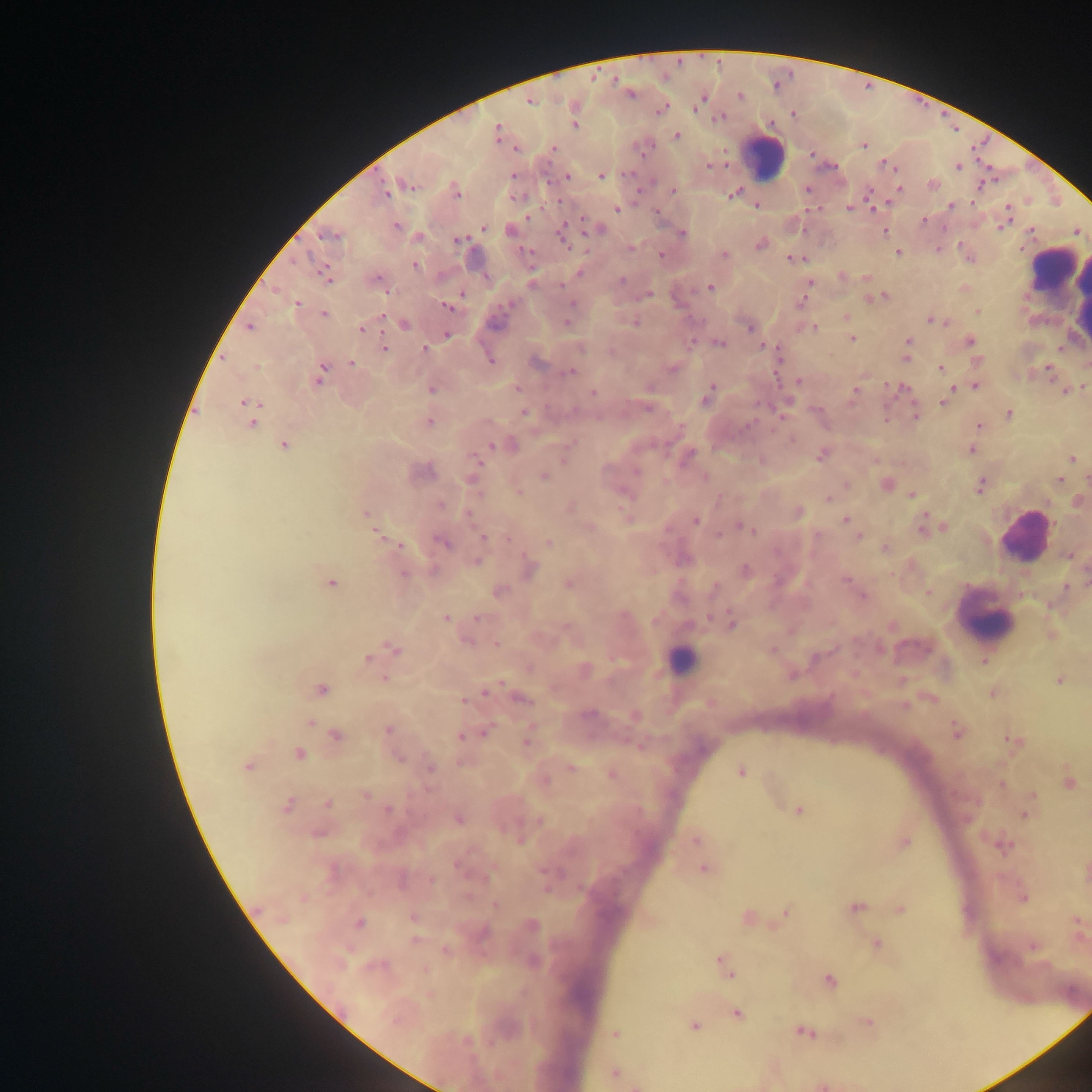

Approximate centers as x y in pixels. Malaria parasite locations: 630 94; 529 101; 662 109; 573 116; 718 117; 574 124; 497 133; 676 135; 863 144; 552 148; 811 154; 958 166; 567 176; 601 176; 407 184; 933 185; 672 190; 898 190; 456 191; 733 193; 756 205; 952 206; 850 208; 616 209; 1007 209; 924 221; 1004 222; 396 226; 483 227; 596 229; 510 230; 884 231; 562 232; 330 234; 682 234; 418 237; 459 239; 760 244; 898 252; 660 255; 723 255; 968 256; 796 259; 415 265; 325 275; 841 275; 865 278; 376 279; 622 280; 809 283; 710 287; 648 294; 874 297; 801 301; 296 304; 449 306; 978 312; 324 313; 845 317; 568 320; 931 320; 403 323; 249 326; 750 327; 361 328; 812 328; 446 334; 851 338; 908 341; 970 341; 717 342; 384 347; 579 347; 424 349; 906 356; 490 358; 977 360; 352 363; 940 368; 672 369; 1048 370; 569 372; 321 374; 797 382; 975 386; 1083 386; 517 387; 430 388; 899 388; 1066 390; 854 391; 593 393; 708 394; 947 397; 943 401; 249 405; 647 406; 525 412; 1008 414; 915 415; 251 419; 429 422; 979 426; 791 440; 283 444; 509 445; 971 449; 822 454; 686 456; 1072 459; 761 460; 476 461; 420 470; 543 475; 473 479; 1059 479; 886 484; 845 485; 980 485; 519 490; 912 494; 828 498; 1078 501; 569 507; 798 512; 364 514; 695 520; 845 520; 849 521; 744 526; 924 526; 589 527; 943 527; 375 531; 857 535; 483 537; 443 542; 548 543; 398 545; 885 547; 1068 555; 476 562; 529 569; 745 571; 846 580; 330 583; 568 583; 714 588; 1065 589; 498 591; 929 593; 862 595; 445 617; 731 622; 891 625; 1051 634; 467 639; 496 644; 393 649; 367 659; 984 660; 583 670; 791 674; 385 678; 1058 679; 321 689; 487 690; 992 692; 520 698; 927 698; 464 701; 587 714; 634 714; 309 723; 387 730; 956 730; 484 731; 469 734; 336 736; 461 736; 526 739; 1012 741; 638 745; 298 753; 398 757; 247 766; 429 767; 571 767; 740 771; 610 773; 543 780; 1067 782; 1001 784; 364 794; 1032 795; 327 803; 285 805; 388 809; 798 809; 1024 814; 458 818; 318 832; 695 839; 904 842; 1002 844; 459 865; 703 868; 1022 897; 495 904; 855 907; 900 909; 785 912; 413 918; 747 918; 1076 921; 358 923; 531 925; 481 932; 415 939; 875 944; 1032 945; 446 950; 722 963; 828 981; 736 1012; 867 1022; 693 1025; 803 1031; 615 1033; 614 1072; 821 1085; 638 1086. Leukocyte locations: 762 157; 1052 268; 1059 288; 1021 534; 985 616; 681 661; 1073 994. Image is 1092×1092 pixels. Thick blood smear. Collected in Ghana. Mobile-phone photograph taken through the microscope. One field of view.